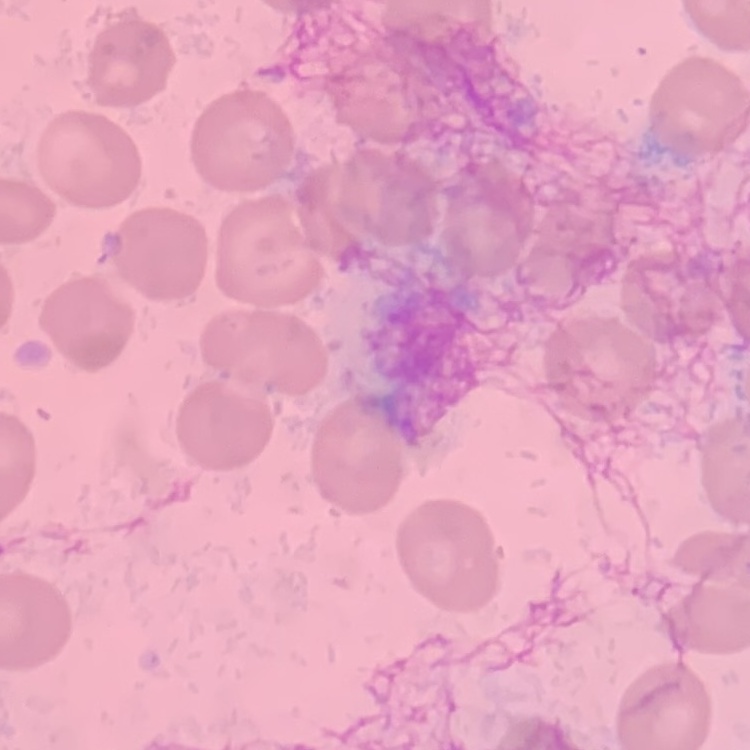
Summary:
  - Red blood cell morphology: no rouleaux formation
  - Image type: square crop of a larger photomicrograph
  - Preparation: thin peripheral smear
  - Stain: Field's or Giemsa